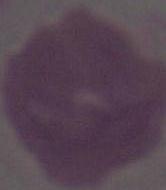

magnification = 1000x
modality = micrograph
identification = red blood cell